Describe the morphology of the red blood cells.
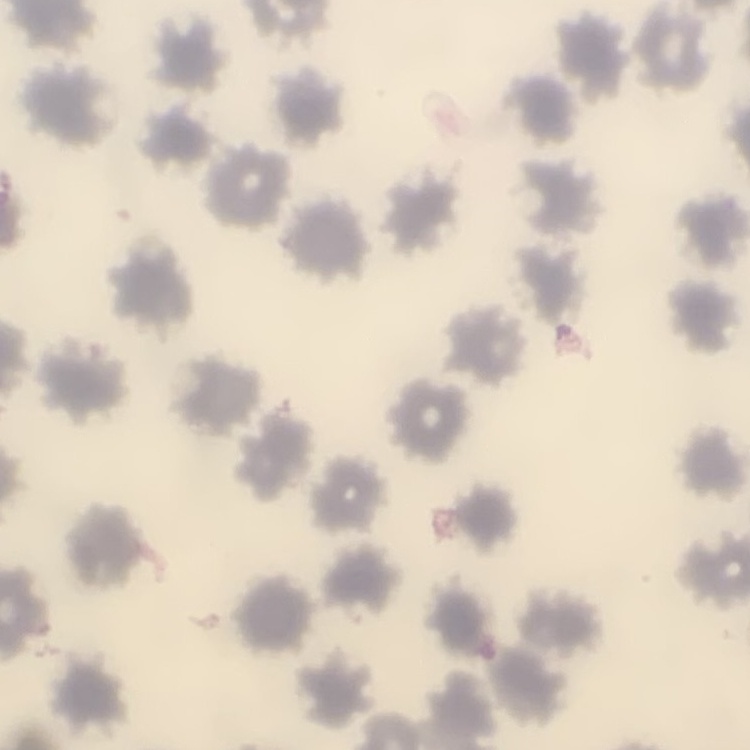
No rouleaux formation.

One tile cut from a larger photomicrograph. Stained with either Field's or Giemsa. Thin blood smear.